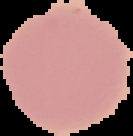
image type = segmented cell region on a black background
preparation = thin blood film
image size = 133×136 pixels
malaria status = uninfected